Comment on the morphology of the red blood cells.
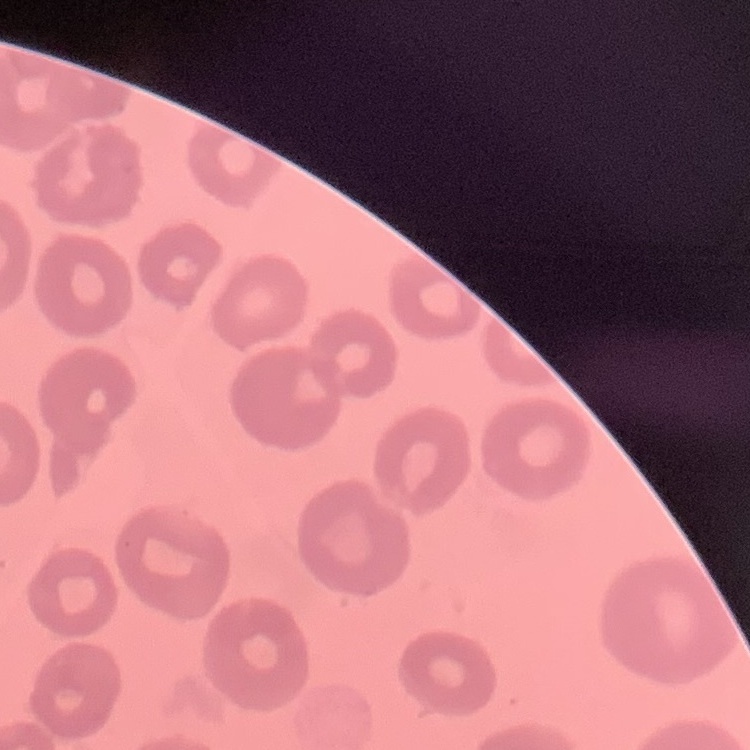

No rouleaux formation.

Square crop of a larger photomicrograph. Stained with either Field's or Giemsa. Thin blood film.